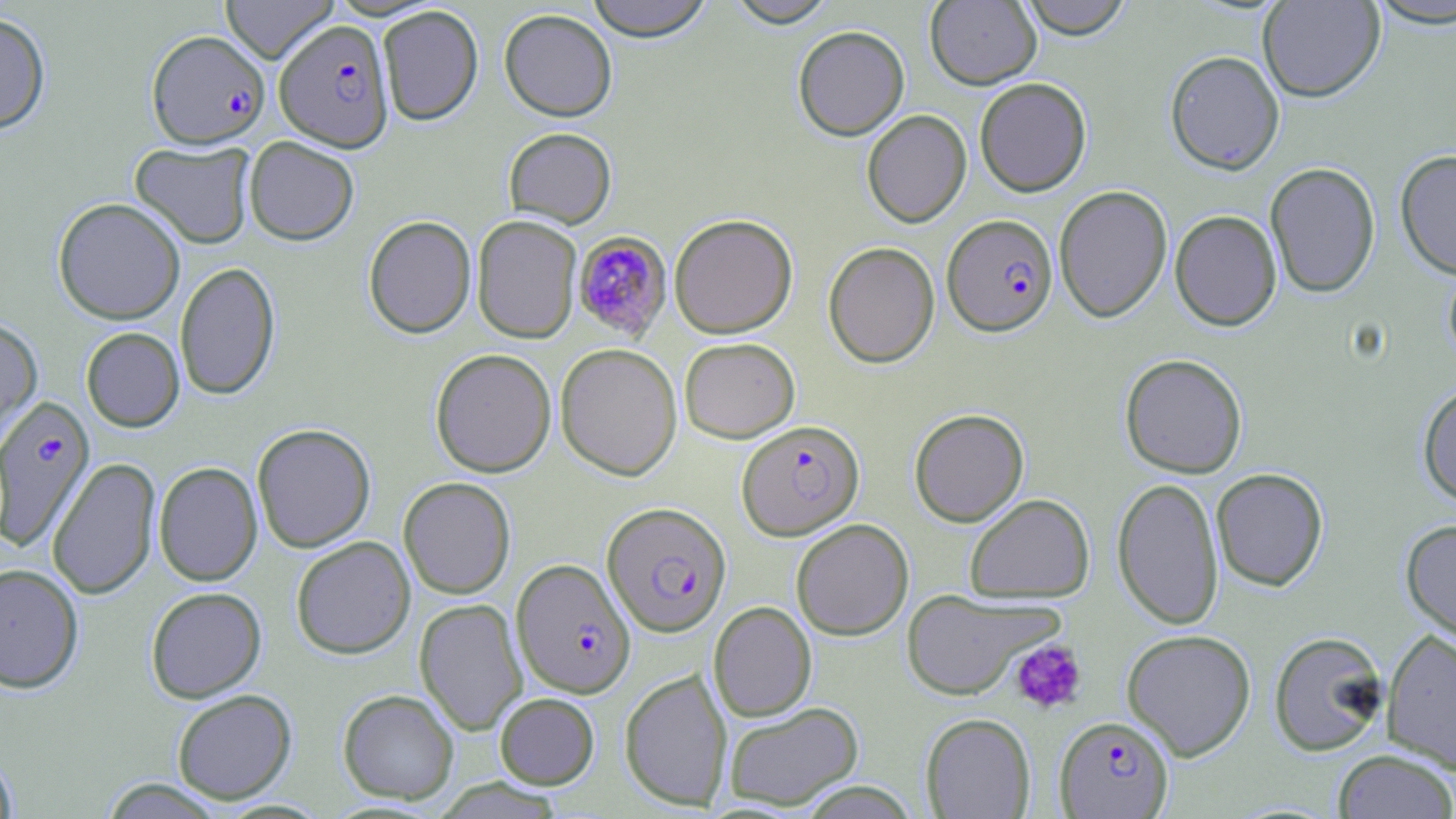

slide-level diagnosis = Plasmodium falciparum
preparation = thin blood smear
image size = 1456×819 pixels
modality = optical microscopy
uninfected red blood cell locations = approximate bounding boxes as (x1, y1, x2, y2) in pixels: (220, 0, 339, 63), (584, 0, 715, 41), (724, 0, 840, 28), (925, 0, 1041, 89), (1018, 0, 1133, 38), (1258, 0, 1385, 102), (1365, 1, 1456, 29), (377, 5, 483, 125), (499, 8, 618, 121), (0, 10, 51, 135), (792, 25, 910, 141), (1165, 50, 1284, 174), (975, 77, 1091, 196), (862, 109, 971, 227), (503, 127, 617, 228), (244, 136, 359, 245), (130, 142, 255, 249), (1395, 149, 1456, 279), (1264, 162, 1381, 298), (1054, 185, 1173, 322), (53, 197, 186, 324), (1169, 210, 1282, 331), (669, 213, 798, 339), (472, 215, 582, 343), (363, 216, 476, 339), (823, 241, 940, 368), (1443, 259, 1456, 368), (174, 262, 281, 400), (0, 317, 42, 447), (80, 327, 184, 432), (679, 337, 800, 442), (556, 344, 682, 481), (430, 348, 556, 477), (1120, 353, 1248, 478), (1417, 383, 1456, 507), (909, 408, 1029, 527), (252, 423, 376, 552), (47, 457, 161, 599), (153, 461, 263, 586), (1211, 467, 1328, 591), (398, 477, 516, 599), (1112, 477, 1224, 630), (964, 493, 1095, 603), (1400, 518, 1456, 645), (791, 519, 913, 640), (291, 536, 415, 659), (0, 563, 84, 693), (145, 586, 266, 703), (901, 589, 1057, 700), (415, 598, 527, 735), (709, 602, 817, 721), (1381, 627, 1456, 774), (1121, 629, 1257, 761), (1268, 631, 1388, 756), (619, 668, 733, 811), (172, 689, 297, 804), (337, 689, 459, 804), (495, 692, 599, 789), (723, 701, 864, 811), (920, 713, 1036, 818), (1332, 749, 1456, 819), (0, 750, 18, 818), (97, 778, 229, 818)
platelet locations = approximate bounding boxes as (x1, y1, x2, y2) in pixels: (1010, 638, 1087, 714)
magnification = 1000x
stain = May-Grünwald-Giemsa
field of view = one of a larger specimen
Plasmodium falciparum-infected red blood cell locations = approximate bounding boxes as (x1, y1, x2, y2) in pixels: (275, 19, 393, 152), (147, 29, 271, 148), (942, 214, 1058, 336), (571, 230, 674, 342), (1, 395, 95, 552), (737, 420, 864, 540), (602, 502, 731, 637), (512, 559, 636, 698), (1054, 715, 1174, 818)